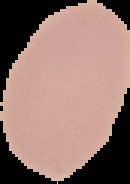
image_type: segmented cell region with the area outside set to black
image_size: 130×184 pixels
preparation: thin blood film
result: no malaria parasites seen